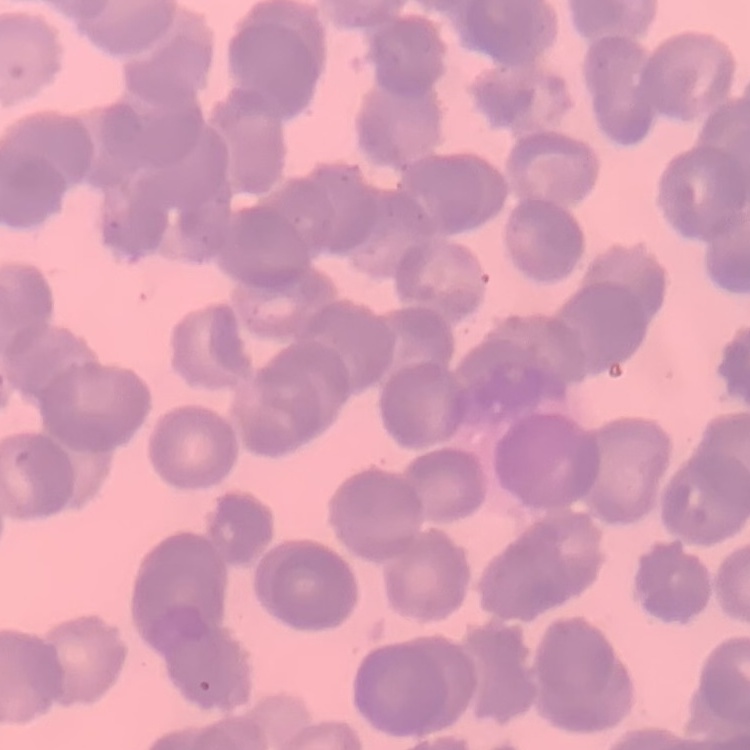 The erythrocytes show rouleaux formation. Thin blood film. Square crop of a larger photomicrograph. Stained with either Field's or Giemsa.